Assess this cell for malaria.
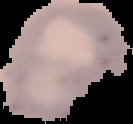

It is uninfected.

Cell region segmented out of the field of view; the surrounding area is masked to black. Image is 133×124 pixels. From a thin blood smear.